Assess this cell for malaria.
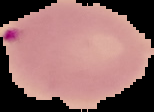

Parasitized.

image type = segmented cell region on a black background
image size = 154×112 pixels
preparation = thin blood film